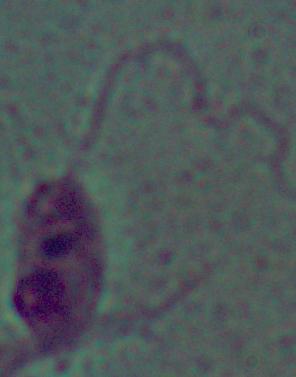

magnification = 1000x
identification = Leishmania
modality = photomicrograph